Report the malaria status of this cell.
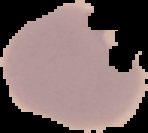
It is parasitized.

Summary:
  - Image size: 148×133 pixels
  - Preparation: thin blood smear
  - Image type: segmented cell region with the area outside set to black